Report the malaria status of this cell.
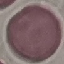

It is uninfected.

Automatically extracted cell patch, resized to 64 × 64 pixels. Thin blood smear. Acquired by smartphone through the microscope eyepiece. Giemsa stain.